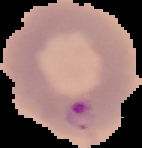
{
  "preparation": "thin blood film",
  "image_type": "segmented cell region with the area outside set to black",
  "malaria_status": "parasitized",
  "image_size": "142×148 pixels"
}